Classify this cell by malaria status.
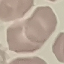

It is uninfected.

image type = automatically extracted cell patch, resized to 64 × 64 pixels
capture = smartphone through the microscope eyepiece
preparation = thin blood film
stain = Giemsa